Name the cell type shown.
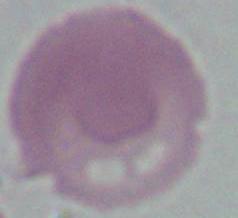
This is an erythrocyte.

{
  "modality": "micrograph",
  "magnification": "1000x"
}